Locate every blood parasite and identify its species.
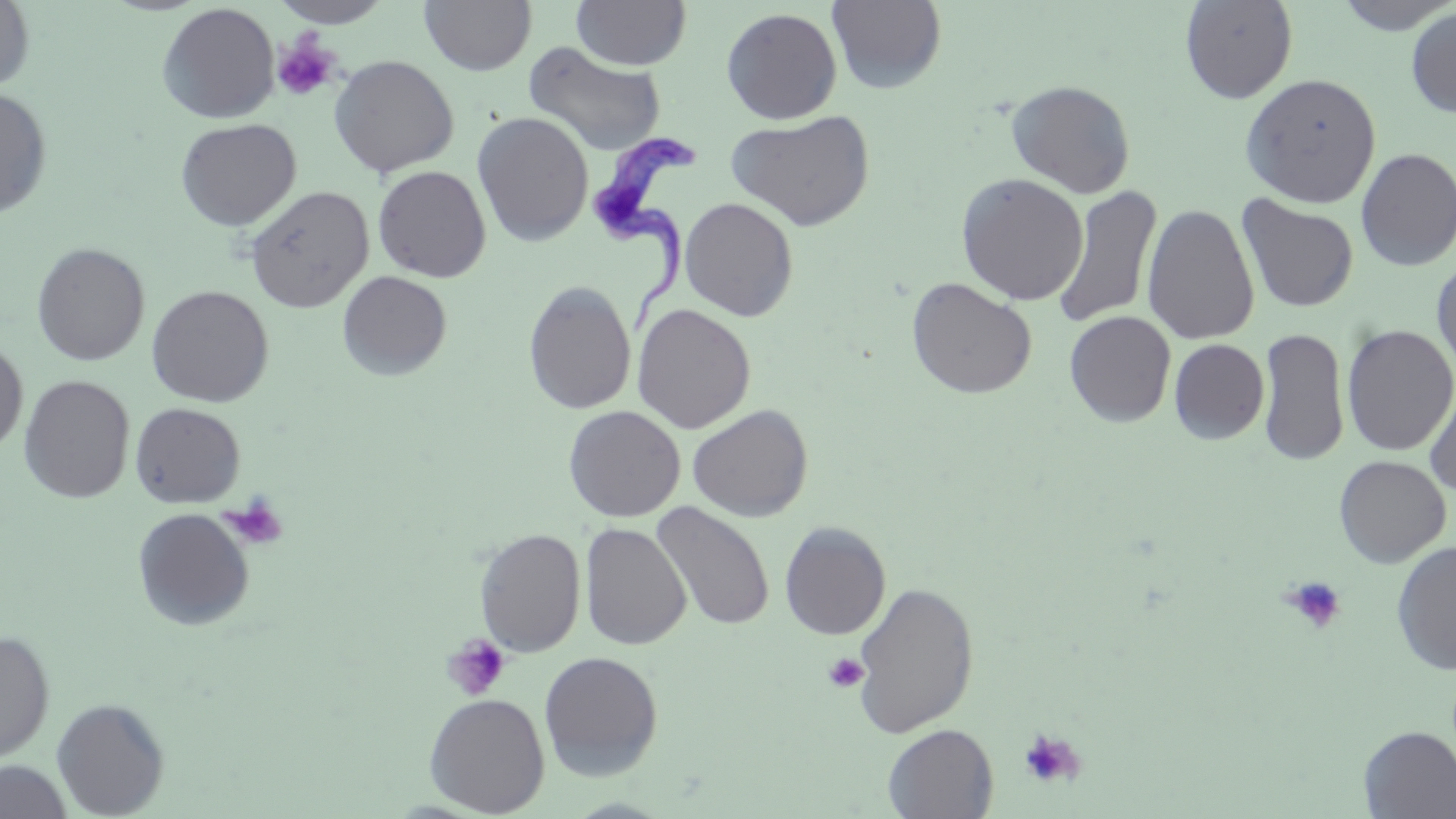

Approximate bounding boxes as (x1, y1, x2, y2) in pixels.
Trypanosoma brucei: (588, 128, 701, 336).
No Plasmodium falciparum, Plasmodium ovale, Plasmodium malariae, Plasmodium vivax, or Babesia divergens observed.

Summary:
  - Platelet locations: (272, 33, 341, 102), (219, 495, 289, 551), (1281, 575, 1348, 634), (442, 633, 511, 701), (823, 652, 869, 694), (1018, 728, 1086, 789)
  - Uninfected red blood cell locations: (0, 0, 36, 93), (270, 0, 392, 28), (419, 0, 536, 76), (571, 0, 691, 70), (827, 0, 947, 94), (1180, 0, 1298, 104), (1333, 0, 1455, 35), (157, 3, 279, 124), (721, 7, 843, 124), (1406, 7, 1456, 119), (523, 42, 666, 157), (329, 54, 459, 178), (1240, 73, 1381, 208), (1006, 79, 1136, 197), (0, 88, 53, 220), (726, 110, 875, 231), (472, 111, 594, 246), (175, 118, 302, 231), (1355, 147, 1456, 271), (372, 165, 491, 282), (956, 173, 1089, 306), (245, 185, 374, 312), (1052, 186, 1163, 330), (1237, 195, 1359, 312), (680, 197, 799, 321), (1142, 203, 1260, 345), (31, 242, 150, 366), (1431, 257, 1456, 384), (337, 270, 452, 380), (906, 277, 1037, 399), (523, 281, 636, 415), (146, 285, 274, 407), (632, 303, 756, 433), (1064, 310, 1177, 427), (1341, 325, 1456, 456), (1257, 327, 1349, 466), (1169, 338, 1270, 444), (0, 340, 28, 454), (19, 375, 135, 503), (1425, 377, 1456, 499), (130, 402, 246, 508), (687, 404, 813, 522), (563, 405, 685, 522), (1333, 455, 1451, 567), (652, 502, 775, 632), (132, 507, 255, 631), (580, 521, 691, 650), (779, 521, 891, 639), (474, 526, 586, 657), (1391, 540, 1456, 675), (852, 580, 979, 739), (0, 630, 55, 764), (538, 651, 664, 780), (423, 692, 550, 816), (51, 698, 169, 818), (882, 723, 998, 819), (1358, 726, 1456, 818), (0, 760, 73, 819)
  - Slide-level diagnosis: Trypanosoma brucei
  - Field of view: one of a larger specimen
  - Modality: optical microscopy
  - Image size: 1456×819 pixels
  - Preparation: thin blood smear
  - Magnification: 1000x
  - Stain: May-Grünwald-Giemsa